Name the cell type shown.
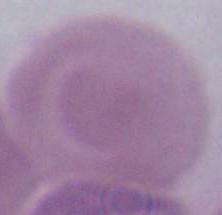
An erythrocyte.

Photomicrograph. 1000x magnification.